Assess this cell for malaria.
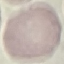
It is uninfected.

Summary:
  - Capture: smartphone camera at the microscope eyepiece
  - Preparation: thin blood smear
  - Image type: automatically extracted cell patch, resized to 64 × 64 pixels
  - Stain: Giemsa